Assess this cell for malaria.
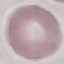

Uninfected.

Thin blood film. Cell patch, automatically extracted from a larger field of view and resized to 64 × 64 pixels. Acquired by smartphone through the microscope eyepiece. Giemsa-stained preparation.